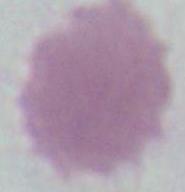

Summary:
  - Magnification: 1000x
  - Modality: photomicrograph
  - Identification: red blood cell